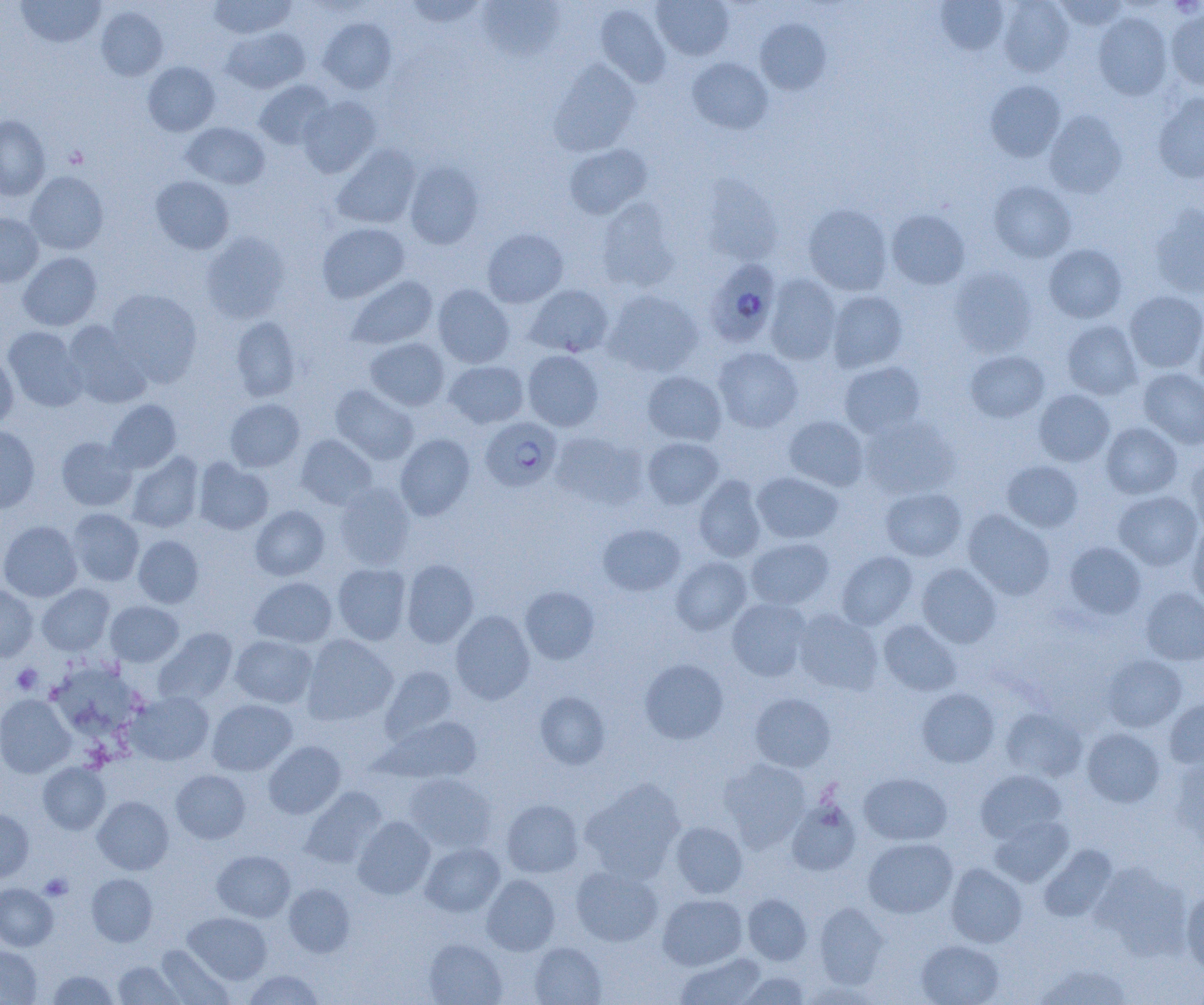

Approximate bounding boxes as named x1/y1/x2/y2 corners in pixels. Uninfected red blood cell locations: (x1=16, y1=0, x2=105, y2=47), (x1=208, y1=0, x2=296, y2=38), (x1=403, y1=0, x2=487, y2=28), (x1=651, y1=0, x2=734, y2=60), (x1=935, y1=0, x2=1009, y2=55), (x1=998, y1=0, x2=1074, y2=76), (x1=1055, y1=0, x2=1128, y2=32), (x1=477, y1=2, x2=566, y2=62), (x1=595, y1=3, x2=671, y2=87), (x1=96, y1=6, x2=168, y2=81), (x1=1166, y1=9, x2=1204, y2=90), (x1=1093, y1=11, x2=1172, y2=100), (x1=319, y1=18, x2=396, y2=93), (x1=755, y1=18, x2=831, y2=94), (x1=221, y1=27, x2=310, y2=93), (x1=687, y1=57, x2=773, y2=134), (x1=549, y1=60, x2=641, y2=157), (x1=142, y1=61, x2=220, y2=136), (x1=254, y1=80, x2=334, y2=150), (x1=985, y1=80, x2=1065, y2=161), (x1=1153, y1=92, x2=1204, y2=183), (x1=297, y1=96, x2=382, y2=178), (x1=1044, y1=110, x2=1127, y2=198), (x1=0, y1=115, x2=50, y2=200), (x1=182, y1=122, x2=270, y2=190), (x1=332, y1=144, x2=421, y2=229), (x1=564, y1=144, x2=652, y2=219), (x1=405, y1=161, x2=484, y2=249), (x1=25, y1=171, x2=109, y2=255), (x1=150, y1=176, x2=234, y2=254), (x1=699, y1=176, x2=783, y2=266), (x1=989, y1=180, x2=1076, y2=262), (x1=596, y1=197, x2=681, y2=292), (x1=803, y1=203, x2=893, y2=295), (x1=1148, y1=205, x2=1204, y2=298), (x1=886, y1=209, x2=970, y2=289), (x1=0, y1=213, x2=43, y2=287), (x1=317, y1=223, x2=410, y2=303), (x1=482, y1=228, x2=568, y2=307), (x1=201, y1=232, x2=290, y2=324), (x1=1044, y1=243, x2=1127, y2=323), (x1=18, y1=252, x2=102, y2=330), (x1=949, y1=266, x2=1037, y2=356), (x1=765, y1=273, x2=842, y2=365), (x1=346, y1=275, x2=438, y2=350), (x1=433, y1=284, x2=514, y2=368), (x1=525, y1=284, x2=613, y2=357), (x1=107, y1=288, x2=202, y2=386), (x1=603, y1=289, x2=703, y2=377), (x1=826, y1=290, x2=908, y2=372), (x1=1124, y1=290, x2=1204, y2=373), (x1=230, y1=316, x2=301, y2=402), (x1=1192, y1=316, x2=1204, y2=393), (x1=1062, y1=320, x2=1142, y2=399), (x1=64, y1=321, x2=152, y2=408), (x1=3, y1=326, x2=87, y2=412), (x1=365, y1=337, x2=450, y2=411), (x1=713, y1=347, x2=803, y2=433), (x1=522, y1=350, x2=604, y2=431), (x1=965, y1=350, x2=1049, y2=422), (x1=0, y1=351, x2=18, y2=428), (x1=443, y1=360, x2=529, y2=429), (x1=839, y1=361, x2=925, y2=438), (x1=1138, y1=367, x2=1204, y2=448), (x1=643, y1=371, x2=727, y2=445), (x1=331, y1=385, x2=419, y2=464), (x1=1034, y1=389, x2=1114, y2=466), (x1=225, y1=398, x2=305, y2=472), (x1=106, y1=399, x2=182, y2=472), (x1=784, y1=415, x2=869, y2=490), (x1=859, y1=415, x2=960, y2=499), (x1=1101, y1=423, x2=1182, y2=499), (x1=0, y1=424, x2=41, y2=513), (x1=550, y1=432, x2=647, y2=510), (x1=295, y1=434, x2=377, y2=510), (x1=395, y1=434, x2=475, y2=520), (x1=56, y1=436, x2=137, y2=511), (x1=642, y1=437, x2=723, y2=509), (x1=127, y1=452, x2=204, y2=533), (x1=1186, y1=455, x2=1204, y2=534), (x1=193, y1=458, x2=273, y2=535), (x1=1002, y1=460, x2=1083, y2=533), (x1=752, y1=472, x2=843, y2=544), (x1=693, y1=475, x2=767, y2=562), (x1=334, y1=482, x2=416, y2=569), (x1=880, y1=487, x2=966, y2=561), (x1=1113, y1=490, x2=1203, y2=571), (x1=250, y1=505, x2=330, y2=581), (x1=67, y1=508, x2=144, y2=586), (x1=963, y1=510, x2=1055, y2=599), (x1=0, y1=520, x2=82, y2=602), (x1=1187, y1=521, x2=1204, y2=609), (x1=598, y1=523, x2=685, y2=596), (x1=133, y1=535, x2=204, y2=608), (x1=745, y1=537, x2=835, y2=610), (x1=1064, y1=541, x2=1146, y2=619), (x1=836, y1=551, x2=917, y2=630), (x1=671, y1=556, x2=751, y2=634), (x1=401, y1=559, x2=479, y2=647), (x1=332, y1=563, x2=411, y2=645), (x1=917, y1=563, x2=1001, y2=648), (x1=249, y1=576, x2=337, y2=647), (x1=0, y1=584, x2=38, y2=661), (x1=37, y1=584, x2=114, y2=655), (x1=520, y1=586, x2=599, y2=664), (x1=1140, y1=587, x2=1204, y2=665), (x1=727, y1=598, x2=811, y2=680), (x1=105, y1=600, x2=184, y2=667), (x1=793, y1=609, x2=883, y2=695), (x1=451, y1=610, x2=535, y2=704), (x1=878, y1=619, x2=961, y2=695), (x1=154, y1=628, x2=238, y2=705), (x1=302, y1=634, x2=398, y2=725), (x1=230, y1=635, x2=317, y2=708), (x1=1101, y1=654, x2=1186, y2=733), (x1=639, y1=658, x2=728, y2=744), (x1=47, y1=661, x2=145, y2=743), (x1=380, y1=666, x2=457, y2=744), (x1=917, y1=688, x2=1000, y2=767), (x1=126, y1=691, x2=214, y2=765), (x1=535, y1=691, x2=610, y2=769), (x1=750, y1=693, x2=836, y2=772), (x1=0, y1=694, x2=76, y2=777), (x1=207, y1=698, x2=297, y2=776), (x1=1164, y1=698, x2=1204, y2=769), (x1=1001, y1=707, x2=1087, y2=781), (x1=379, y1=716, x2=482, y2=784), (x1=1082, y1=728, x2=1165, y2=807), (x1=263, y1=741, x2=346, y2=818), (x1=719, y1=757, x2=811, y2=849), (x1=1169, y1=759, x2=1204, y2=851), (x1=38, y1=762, x2=110, y2=834), (x1=171, y1=770, x2=251, y2=843), (x1=976, y1=770, x2=1066, y2=844), (x1=859, y1=772, x2=952, y2=845), (x1=403, y1=773, x2=497, y2=852), (x1=580, y1=778, x2=686, y2=882), (x1=301, y1=787, x2=386, y2=867), (x1=93, y1=796, x2=173, y2=875), (x1=786, y1=798, x2=861, y2=876), (x1=502, y1=799, x2=583, y2=878), (x1=0, y1=809, x2=34, y2=881), (x1=989, y1=815, x2=1073, y2=886), (x1=353, y1=816, x2=435, y2=899), (x1=671, y1=822, x2=748, y2=898), (x1=863, y1=838, x2=958, y2=918), (x1=420, y1=842, x2=505, y2=917), (x1=1038, y1=845, x2=1117, y2=922), (x1=212, y1=850, x2=295, y2=922), (x1=945, y1=863, x2=1026, y2=947), (x1=1091, y1=863, x2=1193, y2=958), (x1=571, y1=865, x2=663, y2=947), (x1=87, y1=873, x2=158, y2=946), (x1=482, y1=875, x2=560, y2=956), (x1=0, y1=883, x2=58, y2=950), (x1=284, y1=883, x2=355, y2=957), (x1=1181, y1=889, x2=1204, y2=974), (x1=743, y1=893, x2=812, y2=965), (x1=658, y1=894, x2=748, y2=970), (x1=814, y1=902, x2=889, y2=988), (x1=184, y1=912, x2=272, y2=984), (x1=423, y1=938, x2=506, y2=1005), (x1=916, y1=939, x2=1004, y2=1005), (x1=530, y1=942, x2=606, y2=1005), (x1=156, y1=945, x2=234, y2=1005), (x1=0, y1=946, x2=42, y2=1005), (x1=675, y1=952, x2=766, y2=1005), (x1=113, y1=961, x2=183, y2=1004), (x1=1032, y1=962, x2=1133, y2=1005), (x1=242, y1=969, x2=325, y2=1004), (x1=47, y1=970, x2=119, y2=1004), (x1=737, y1=971, x2=810, y2=1004). Platelet locations: (x1=64, y1=146, x2=87, y2=168), (x1=12, y1=664, x2=42, y2=694), (x1=39, y1=873, x2=73, y2=900). Plasmodium falciparum-infected red blood cell locations: (x1=704, y1=258, x2=781, y2=347), (x1=481, y1=417, x2=562, y2=491). Slide-level diagnosis: Plasmodium falciparum. Image is 1204×1005 pixels. Thin blood smear. 1000x magnification. Light microscopy. One field of a larger specimen.